State the preparation type.
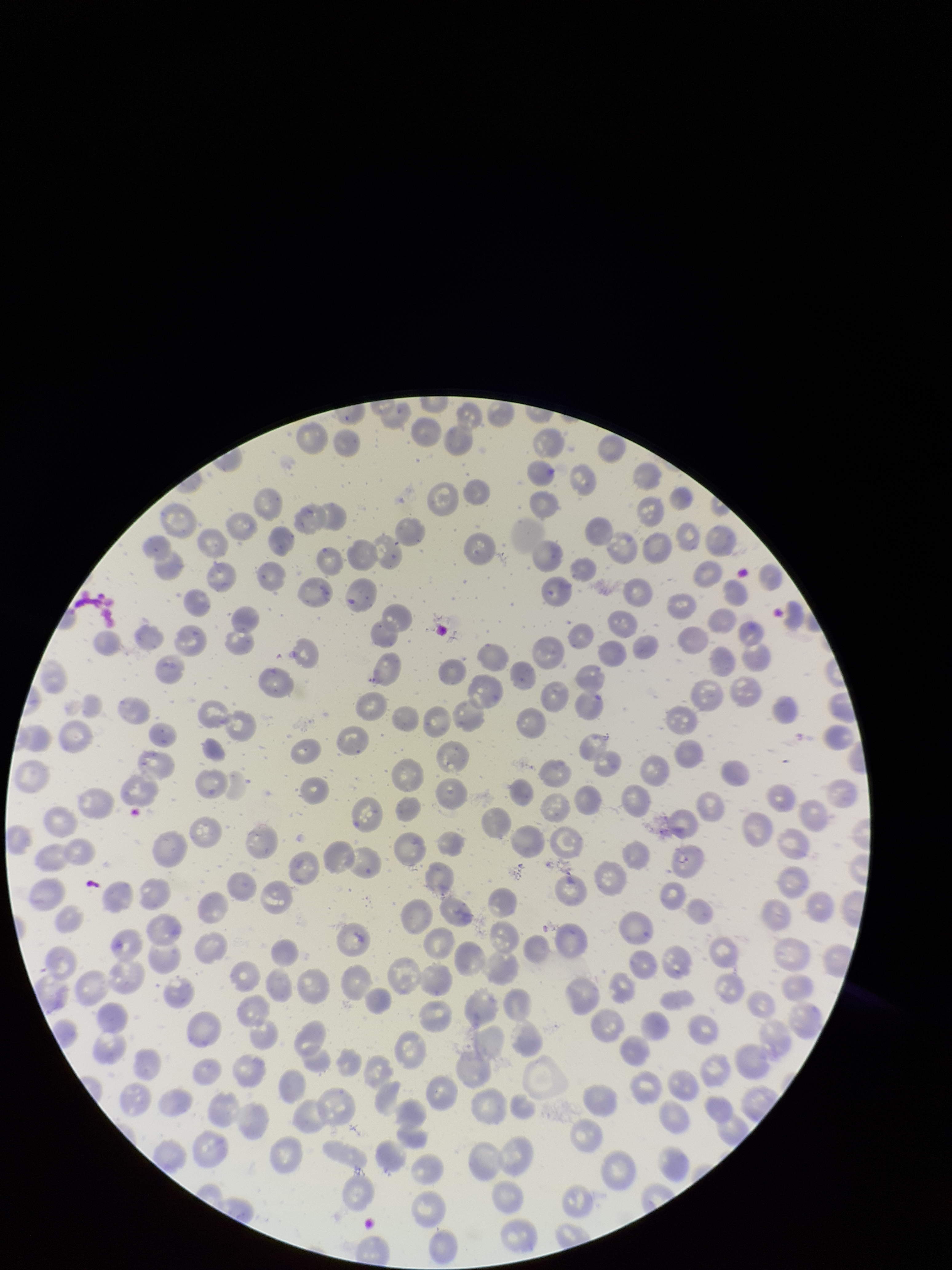

A thin smear.

Summary:
  - Image size: 952×1270 pixels
  - Red blood cell count: 237
  - Parasitized red blood cells: none detected
  - Species reported for this patient: Plasmodium falciparum
  - Capture: smartphone photograph through the microscope eyepiece
  - Stain: Giemsa
  - Field of view: single
  - Patient malaria status: infected
  - Parasitized red blood cell count: 0